Classify this cell by malaria status.
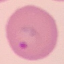
It is parasitized.

Giemsa-stained preparation. Acquired by smartphone through the microscope eyepiece. Thin blood smear. Automatically extracted cell patch, resized to 64 × 64 pixels.